Name the blood parasite species.
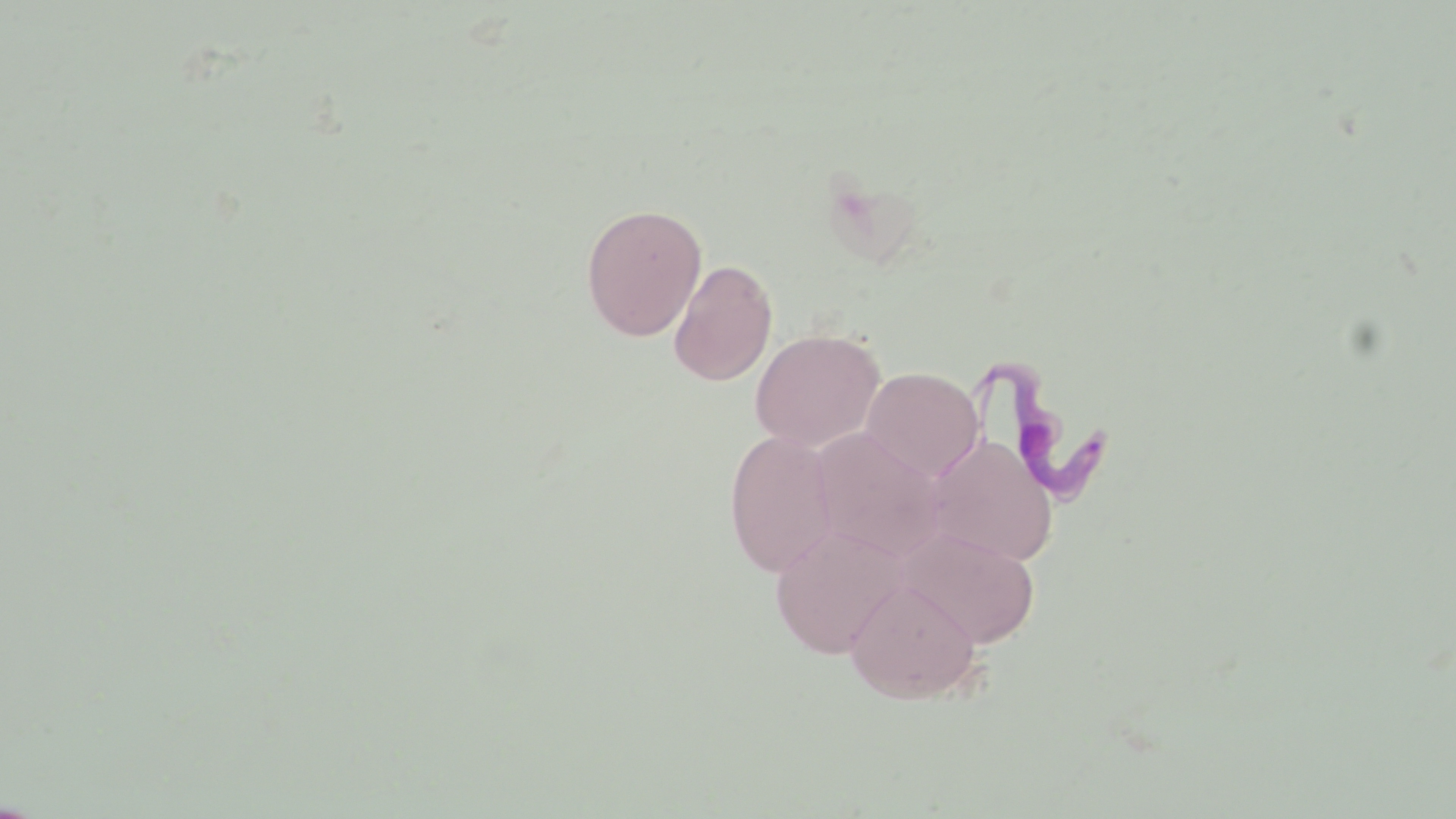
Trypanosoma brucei.

{
  "magnification": "1000x",
  "trypanosoma_brucei_locations": "approximate bounding boxes as (x1, y1, x2, y2) in pixels: (984, 361, 1117, 501)",
  "stain": "May-Grünwald-Giemsa",
  "field_of_view": "one of a larger specimen",
  "preparation": "thin blood film",
  "uninfected_red_blood_cell_locations": "approximate bounding boxes as (x1, y1, x2, y2) in pixels: (580, 203, 707, 342), (668, 259, 778, 386), (750, 328, 885, 451), (860, 367, 985, 482), (809, 427, 946, 562), (723, 429, 838, 577), (924, 434, 1059, 568), (769, 523, 908, 659), (899, 529, 1040, 649), (844, 577, 983, 703)",
  "image_size": "1456×819 pixels",
  "modality": "optical microscopy"
}